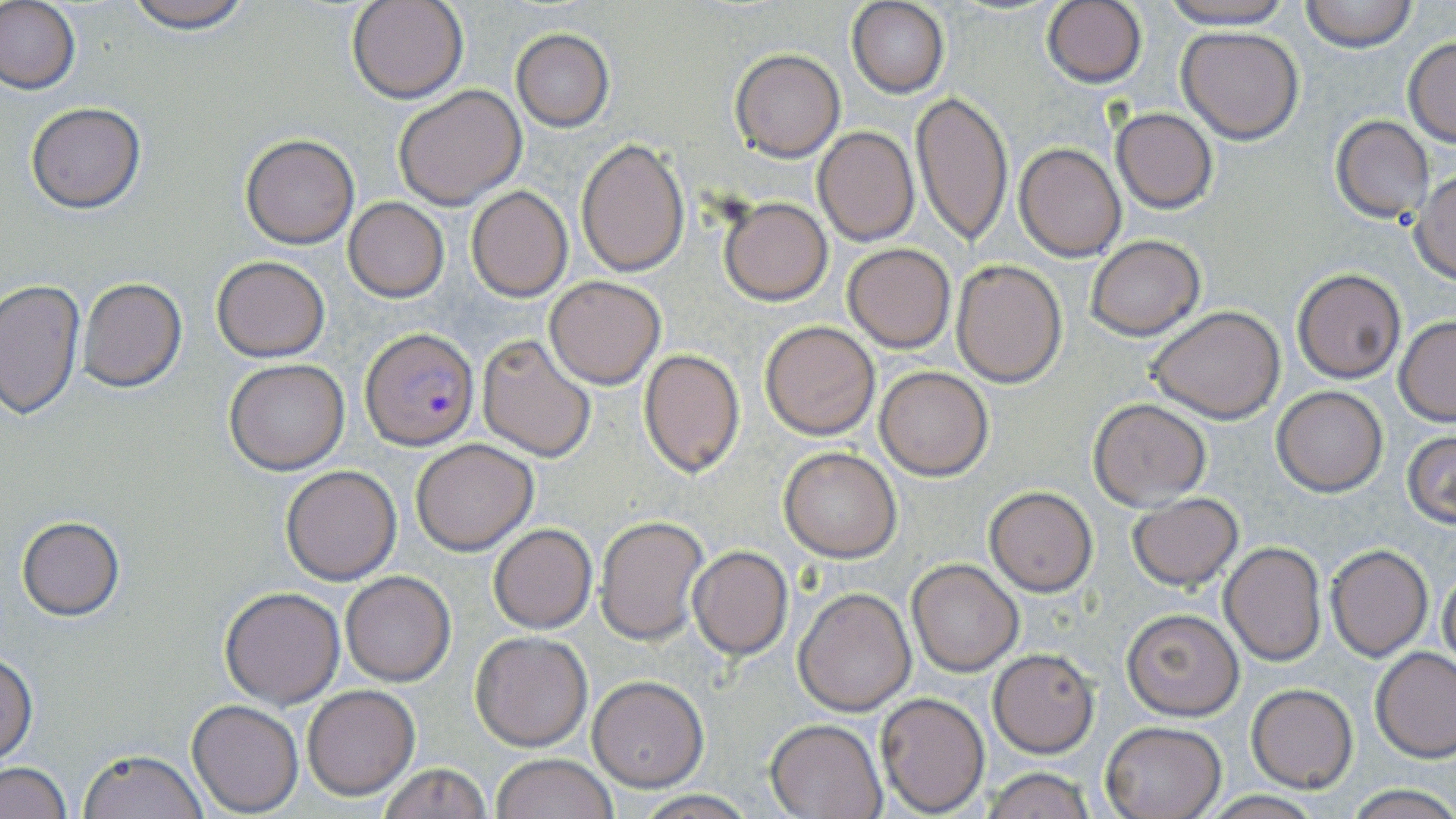

slide-level diagnosis = Plasmodium falciparum
stain = May-Grünwald-Giemsa
magnification = 1000x
preparation = thin blood film
uninfected red blood cell locations = approximate bounding boxes as [x1, y1, x2, y2] in pixels: [0, 0, 81, 96], [116, 0, 258, 33], [347, 0, 469, 103], [1042, 0, 1148, 88], [1154, 0, 1301, 30], [1299, 0, 1418, 52], [847, 2, 948, 97], [1176, 25, 1305, 144], [511, 30, 614, 130], [1403, 37, 1456, 146], [729, 48, 844, 161], [392, 84, 527, 209], [910, 90, 1013, 245], [25, 102, 146, 213], [1111, 107, 1218, 213], [1331, 115, 1435, 221], [814, 127, 918, 245], [239, 134, 360, 248], [573, 138, 689, 275], [1014, 142, 1126, 261], [1409, 171, 1456, 283], [466, 185, 572, 301], [718, 196, 832, 304], [344, 198, 448, 301], [1085, 236, 1205, 340], [843, 243, 956, 352], [211, 255, 330, 361], [951, 260, 1067, 387], [1292, 269, 1407, 383], [545, 275, 666, 389], [77, 277, 188, 392], [0, 278, 84, 418], [1147, 307, 1285, 424], [1394, 317, 1456, 425], [759, 320, 882, 439], [477, 333, 597, 461], [639, 347, 745, 478], [223, 358, 350, 475], [874, 365, 994, 481], [1271, 386, 1387, 496], [1088, 399, 1212, 508], [1403, 430, 1455, 528], [411, 439, 538, 554], [779, 446, 901, 562], [279, 464, 402, 585], [985, 486, 1097, 596], [1127, 492, 1244, 591], [594, 514, 709, 647], [16, 516, 124, 620], [487, 523, 597, 633], [1219, 540, 1326, 665], [1324, 543, 1433, 662], [687, 545, 793, 660], [906, 560, 1024, 676], [1437, 569, 1456, 669], [339, 571, 456, 686], [220, 586, 346, 708], [793, 586, 916, 716], [1122, 609, 1243, 720], [470, 632, 594, 751], [988, 648, 1098, 756], [1373, 648, 1456, 763], [1, 654, 37, 764], [588, 676, 708, 790], [301, 683, 421, 800], [1246, 683, 1359, 792], [877, 692, 990, 814], [187, 699, 304, 816], [766, 717, 887, 818], [1099, 720, 1226, 819], [80, 748, 206, 819], [491, 754, 619, 819], [2, 762, 71, 819], [379, 763, 490, 818], [977, 766, 1098, 819], [1343, 784, 1456, 819], [630, 790, 758, 818], [1198, 793, 1329, 819]
modality = optical microscopy
field of view = one of a larger specimen
Plasmodium falciparum-infected red blood cell locations = approximate bounding boxes as [x1, y1, x2, y2] in pixels: [362, 331, 477, 450]
image size = 1456×819 pixels